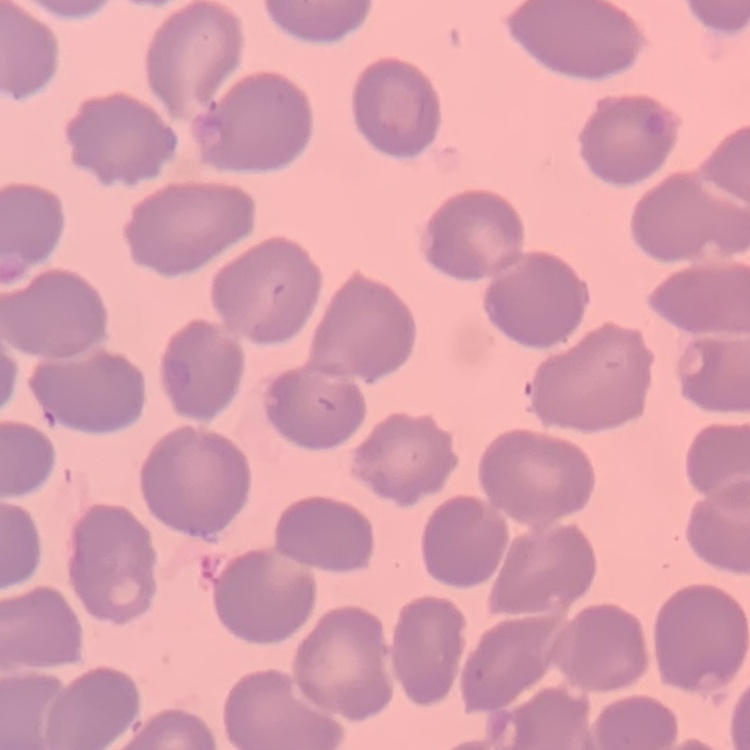

red blood cell morphology = no rouleaux formation
preparation = thin blood film
stain = Field's or Giemsa
image type = square crop of a larger photomicrograph